State the preparation type.
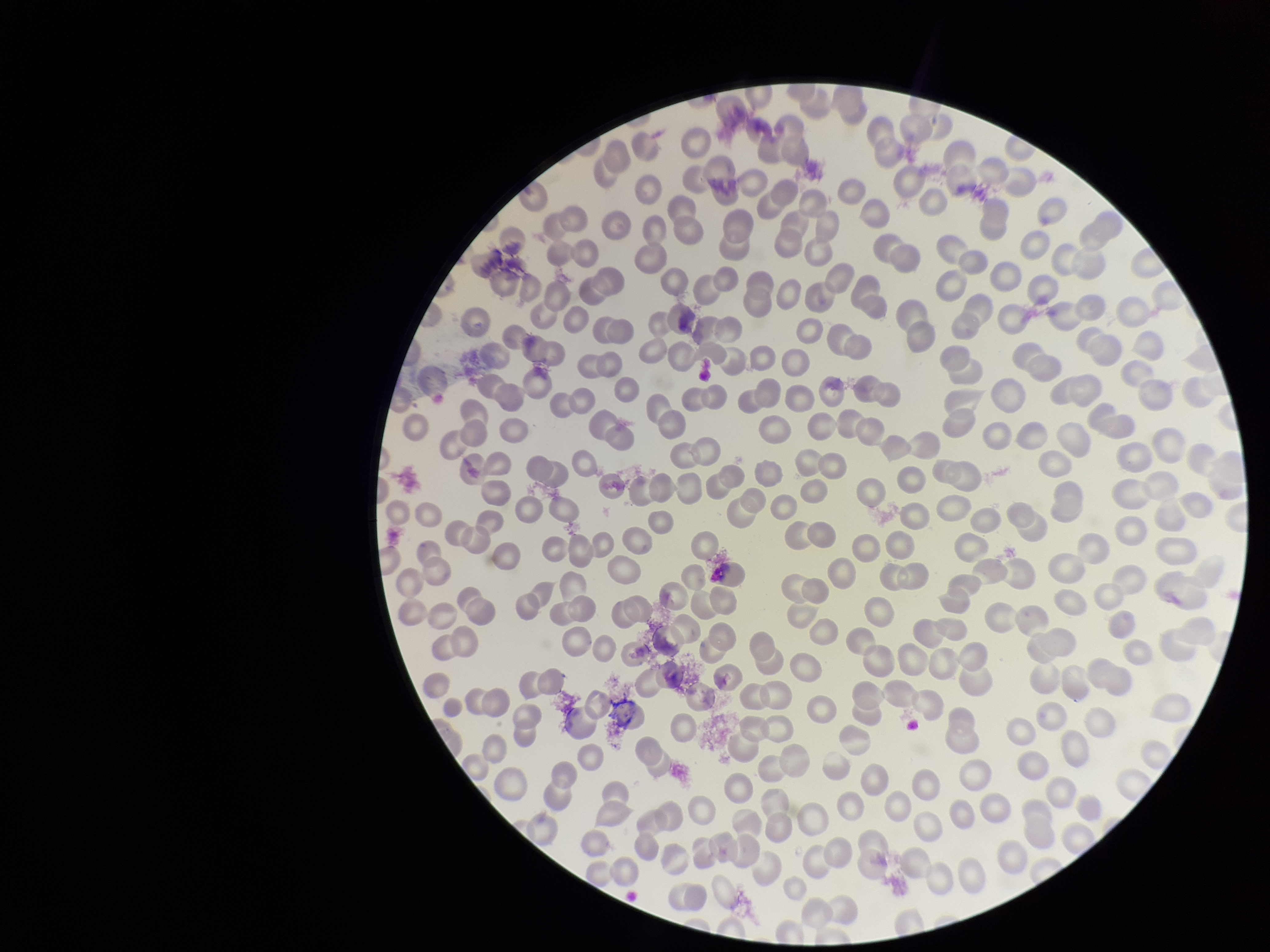

It is a thin blood smear.

Summary:
  - Stain: Giemsa
  - Red blood cell count: 228
  - Parasitized red blood cells: none identified
  - Patient malaria status: negative
  - Image size: 1270×952 pixels
  - Field of view: one from this slide
  - Parasitized red blood cell count: 0
  - Capture: smartphone photograph through the microscope eyepiece